Assess this cell for malaria.
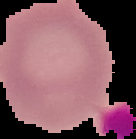

It is uninfected.

Summary:
  - Image size: 136×139 pixels
  - Image type: segmented cell region with the area outside set to black
  - Preparation: thin blood film